Identify the blood parasite species.
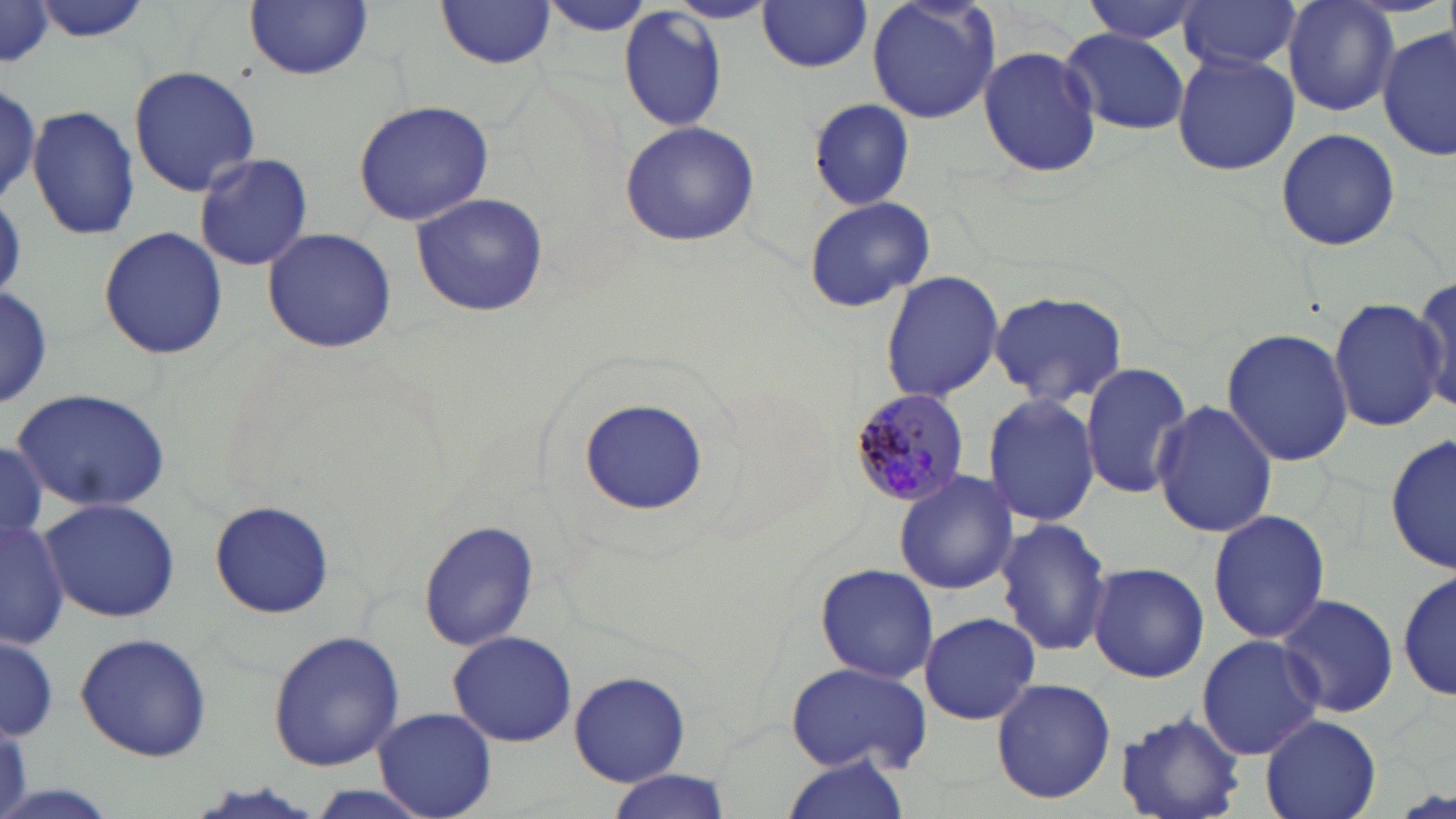
Plasmodium malariae.

Approximate bounding boxes as [x1, y1, x2, y2] in pixels. Uninfected red blood cell locations: [29, 0, 153, 44], [866, 0, 1002, 125], [1081, 0, 1208, 45], [1178, 0, 1301, 73], [1282, 0, 1400, 116], [245, 1, 372, 80], [437, 1, 557, 69], [537, 1, 658, 38], [755, 1, 875, 72], [665, 2, 776, 25], [0, 4, 54, 71], [618, 8, 729, 132], [1377, 25, 1453, 163], [1060, 29, 1189, 134], [979, 44, 1103, 177], [1171, 52, 1300, 175], [127, 64, 262, 195], [0, 75, 44, 209], [0, 81, 43, 203], [807, 99, 914, 210], [353, 100, 494, 227], [25, 104, 140, 240], [618, 120, 761, 247], [1275, 128, 1400, 250], [194, 151, 317, 273], [410, 193, 549, 318], [802, 196, 935, 312], [97, 225, 228, 360], [261, 227, 397, 354], [879, 270, 1004, 401], [1412, 273, 1455, 415], [0, 285, 54, 410], [987, 289, 1130, 408], [1327, 296, 1447, 433], [1222, 328, 1354, 468], [1080, 360, 1193, 501], [9, 389, 174, 512], [980, 392, 1101, 526], [1153, 398, 1278, 540], [580, 399, 706, 514], [1387, 434, 1454, 578], [0, 444, 47, 539], [893, 469, 1021, 593], [39, 499, 182, 623], [209, 502, 334, 618], [1208, 507, 1330, 645], [0, 516, 70, 648], [418, 517, 540, 653], [993, 518, 1114, 657], [1087, 561, 1210, 684], [814, 563, 939, 684], [1398, 566, 1454, 707], [1276, 593, 1398, 718], [918, 612, 1043, 723], [266, 630, 406, 770], [448, 630, 577, 747], [0, 631, 59, 741], [73, 632, 213, 760], [1195, 634, 1324, 760], [787, 661, 934, 776], [570, 669, 692, 786], [990, 678, 1116, 805], [374, 707, 496, 817], [1114, 712, 1247, 819], [1260, 714, 1382, 819], [783, 752, 913, 818], [603, 772, 731, 819]. Plasmodium malariae-infected red blood cell locations: [851, 391, 974, 510]. Thin blood smear. One field of a larger specimen. May-Grünwald-Giemsa stain. Captured at 1000x magnification. Image is 1456×819 pixels. Light microscopy.